Evaluate for Plasmodium parasites.
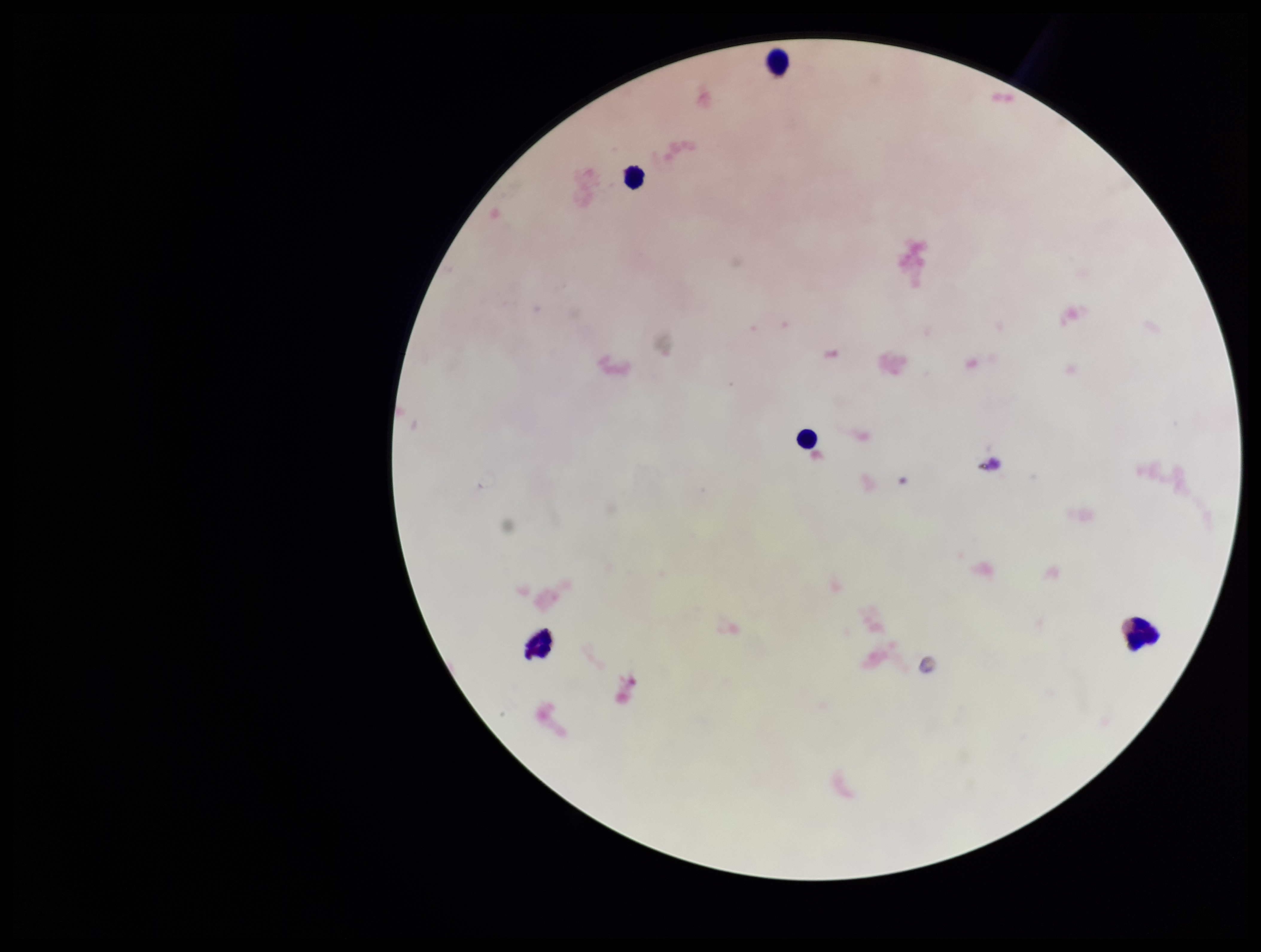
None seen.

leukocyte count = 5
patient malaria status = negative
stain = Giemsa
image size = 1261×952 pixels
parasite count = 0
capture = smartphone photograph through the microscope eyepiece
field of view = single
preparation = thick